Give the position of each P. falciparum parasite with its life-cycle stage, each leukocyte, and any debris.
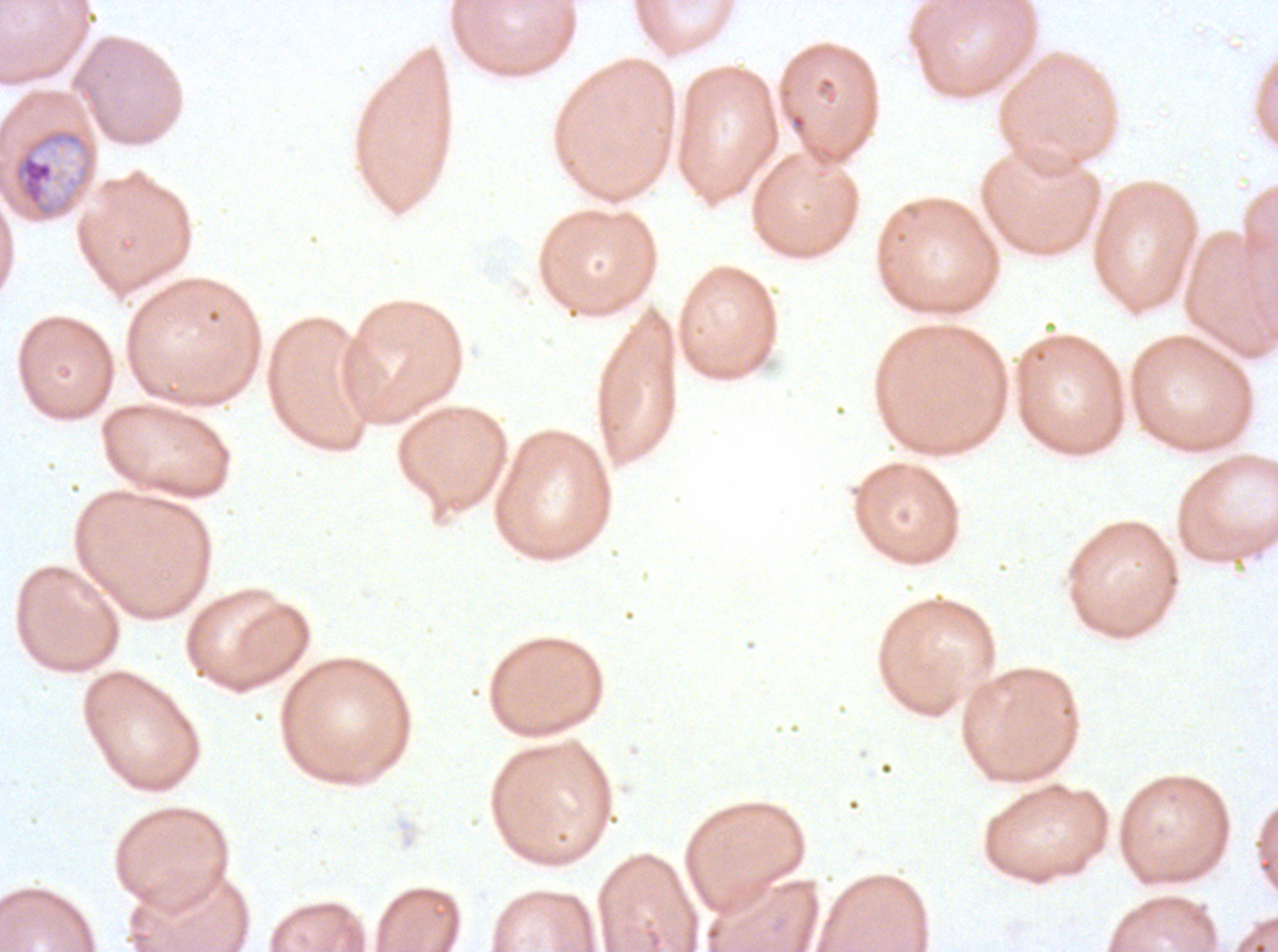

Approximate bounding boxes as {x1, y1, x2, y2} in pixels.
Mid trophozoites: {0, 125, 97, 223}.
No rings, late-ring/early-trophozoite forms, late trophozoites, early schizonts, late schizonts, segmenters, gametocytes, leukocytes, or debris observed.

Summary:
  - Specimen: P. falciparum cultured ex vivo for 24 to 48 hours, from a patient in The Gambia
  - Field of view: one sub-image of a larger composite
  - Image size: 1278×952 pixels
  - Stain: Giemsa
  - Preparation: thin blood film